Classify this cell by malaria status.
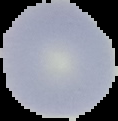

It is uninfected.

Segmented cell region on a black background. Image is 118×121 pixels. From a thin blood smear.